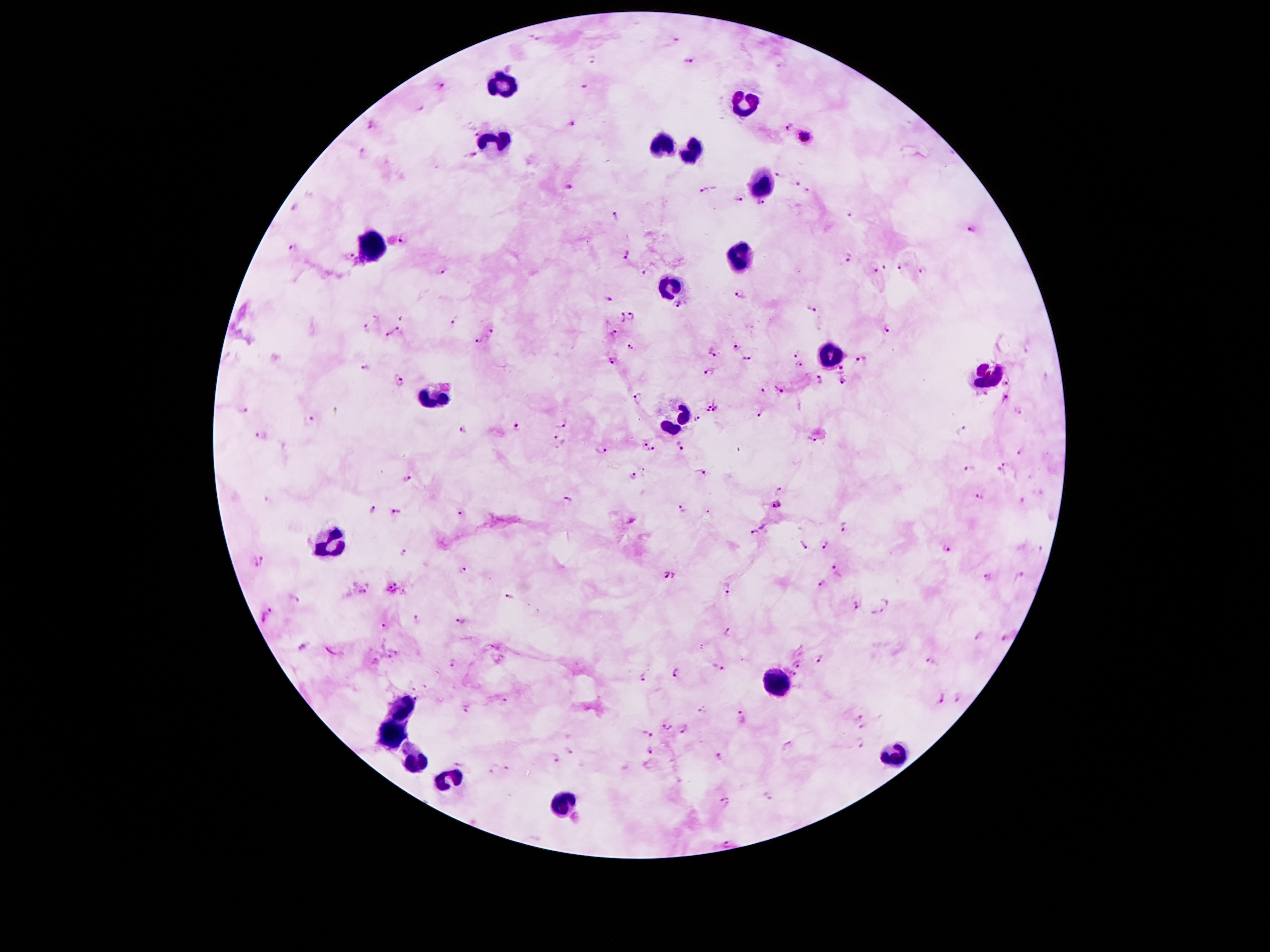

Approximate centers as [x, y] in pixels. Malaria parasite locations: [675, 37], [590, 61], [691, 62], [442, 86], [586, 86], [572, 123], [373, 125], [789, 125], [805, 137], [363, 154], [473, 155], [778, 174], [797, 183], [705, 188], [808, 188], [571, 189], [739, 198], [759, 202], [293, 208], [849, 212], [615, 218], [972, 230], [403, 239], [294, 249], [625, 254], [348, 255], [847, 258], [874, 266], [885, 269], [898, 269], [441, 270], [646, 273], [923, 273], [741, 294], [608, 299], [676, 305], [812, 311], [632, 315], [622, 318], [403, 320], [457, 321], [365, 327], [396, 329], [890, 330], [489, 333], [613, 334], [387, 335], [478, 341], [631, 346], [735, 347], [713, 353], [796, 353], [746, 358], [860, 360], [612, 361], [799, 367], [365, 368], [842, 370], [710, 375], [819, 379], [398, 382], [844, 383], [1008, 383], [780, 389], [763, 391], [638, 397], [1003, 398], [714, 406], [338, 410], [244, 411], [761, 413], [1018, 413], [697, 419], [309, 421], [561, 423], [518, 426], [463, 429], [961, 430], [261, 435], [560, 440], [812, 441], [643, 444], [681, 446], [600, 450], [1023, 450], [652, 451], [1002, 467], [970, 470], [700, 472], [406, 476], [634, 476], [779, 491], [979, 497], [565, 501], [1023, 502], [777, 505], [373, 509], [682, 509], [397, 512], [461, 514], [842, 526], [754, 534], [803, 544], [824, 545], [947, 548], [1041, 550], [403, 553], [264, 561], [254, 563], [839, 569], [464, 572], [668, 576], [1018, 576], [985, 579], [823, 584], [393, 587], [727, 589], [363, 591], [510, 596], [295, 599], [855, 604], [876, 612], [266, 615], [418, 619], [461, 622], [384, 627], [726, 633], [978, 636], [1006, 636], [302, 648], [398, 653], [390, 657], [821, 659], [930, 660], [452, 663], [800, 665], [715, 670], [790, 673], [675, 674], [643, 678], [425, 686], [411, 688], [957, 697], [941, 698], [504, 703], [467, 708], [700, 710], [859, 717], [741, 718], [666, 726], [862, 727], [681, 728], [648, 732], [862, 743], [789, 747], [568, 751], [650, 752], [719, 756], [554, 759], [458, 762], [505, 766], [490, 771], [725, 802], [727, 843]. Leukocyte locations: [501, 87], [747, 101], [497, 144], [663, 146], [692, 152], [756, 185], [370, 244], [739, 259], [668, 285], [831, 353], [987, 376], [434, 398], [676, 421], [335, 539], [776, 683], [405, 707], [391, 734], [897, 757], [417, 765], [442, 779], [559, 804]. 100x magnification. Smartphone photograph taken through the microscope eyepiece. Image is 1270×952 pixels. Thick blood film. One field from this slide. Patient malaria status: positive for Plasmodium falciparum. Giemsa-stained preparation.